Assess this cell for malaria.
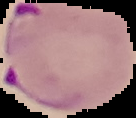
Parasitized.

Summary:
  - Image type: segmented cell region on a black background
  - Image size: 136×118 pixels
  - Preparation: thin blood smear